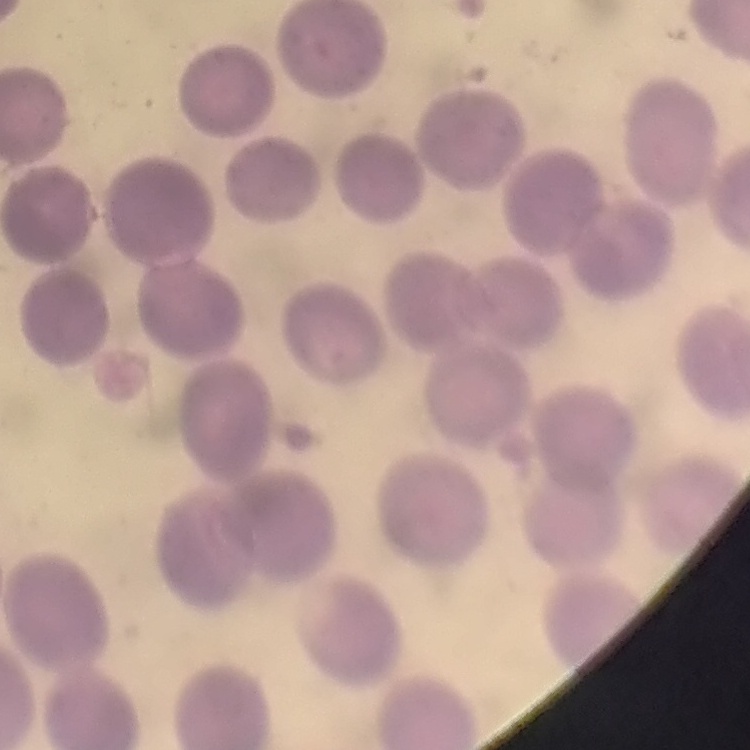
erythrocyte_morphology: no rouleaux formation
image_type: one tile cut from a larger photomicrograph
stain: Field's or Giemsa
preparation: thin blood film